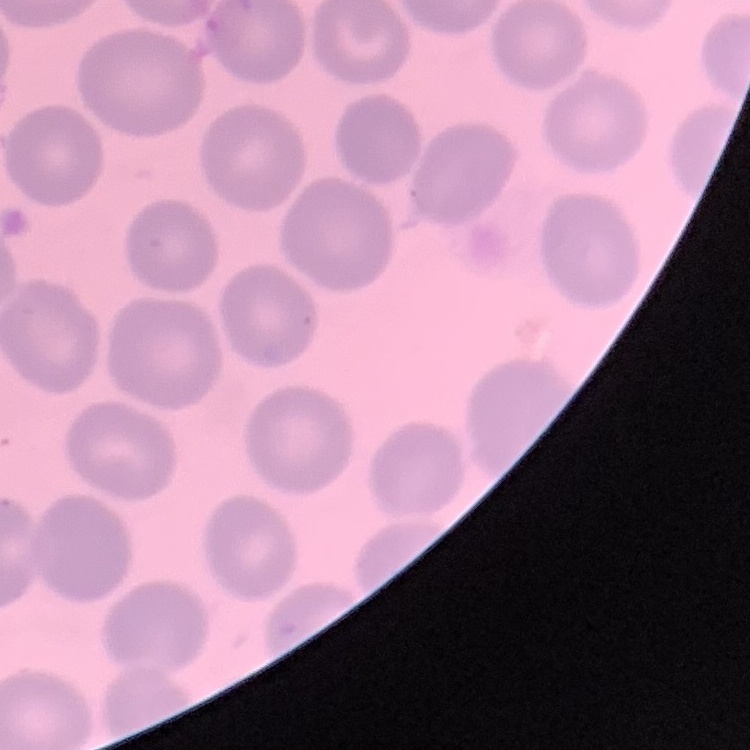
erythrocyte morphology = no rouleaux formation
preparation = thin blood film
stain = Field's or Giemsa
image type = one tile cut from a larger photomicrograph